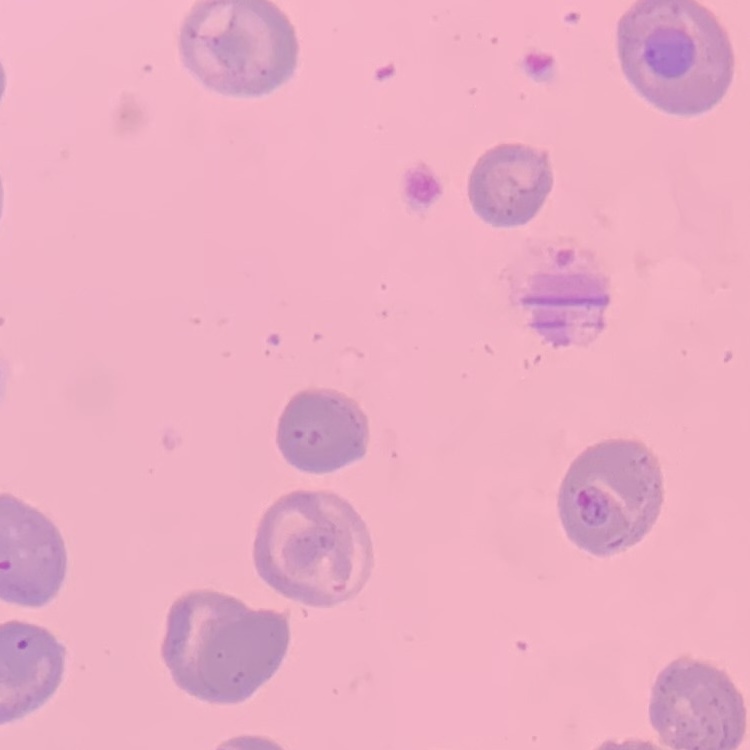

The erythrocytes show no rouleaux formation. One tile cut from a larger photomicrograph. Stained with either Field's or Giemsa. Thin blood smear.